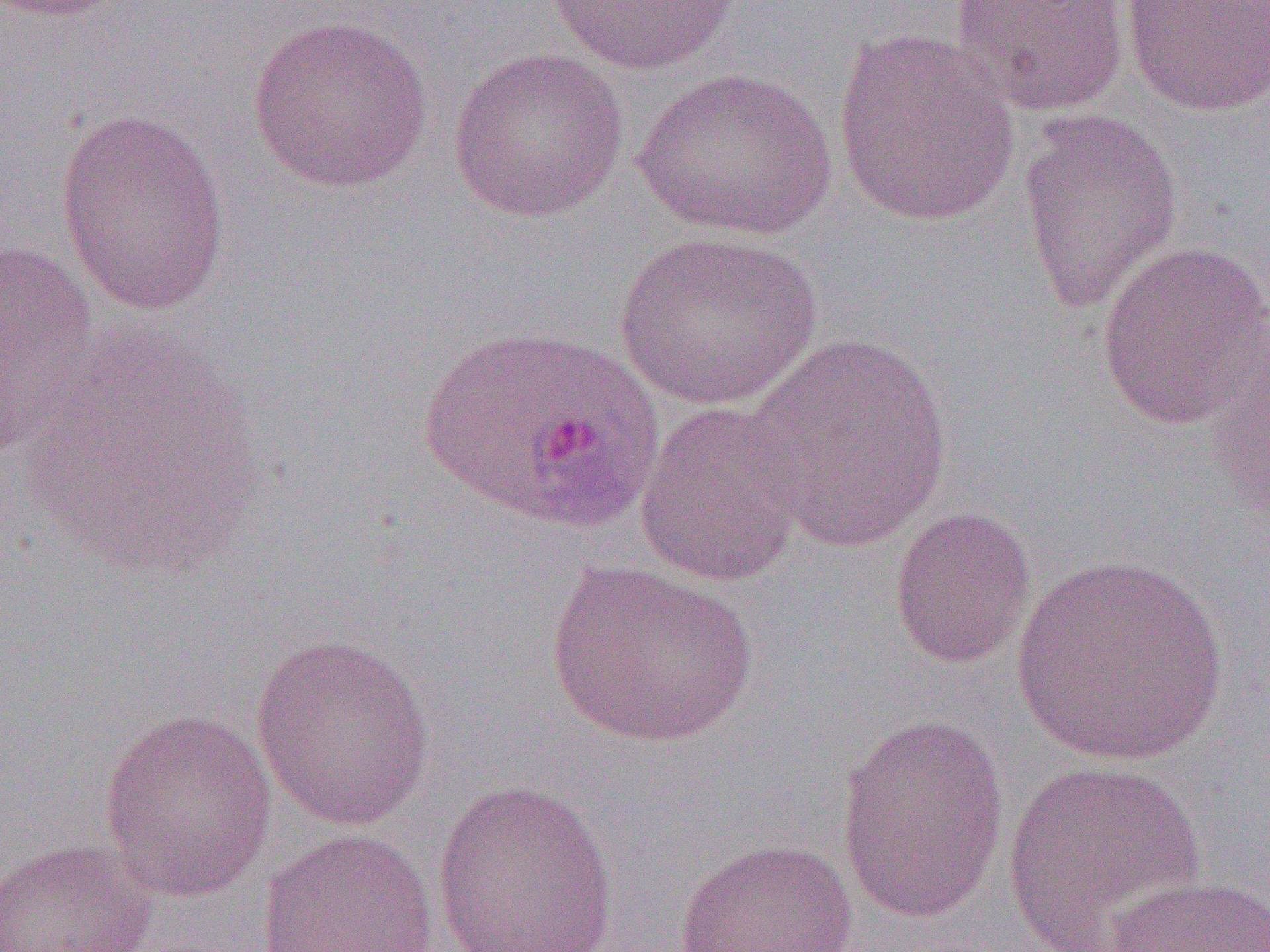

Summary:
  - Coordinate format: approximate bounding boxes as [x1, y1, x2, y2] in pixels
  - Uninfected red blood cell locations: [0, 0, 137, 21], [949, 0, 1130, 118], [1121, 0, 1270, 117], [547, 1, 742, 75], [246, 14, 435, 194], [830, 29, 1022, 229], [447, 46, 630, 223], [632, 66, 839, 242], [1016, 106, 1183, 315], [55, 109, 231, 317], [614, 230, 822, 411], [0, 240, 102, 456], [1096, 240, 1270, 430], [16, 332, 269, 579], [741, 335, 954, 551], [1206, 338, 1270, 525], [634, 400, 811, 590], [888, 505, 1037, 669], [1010, 554, 1230, 766], [541, 559, 761, 749], [249, 633, 436, 832], [100, 706, 278, 902], [835, 712, 1010, 926], [1002, 759, 1207, 950], [431, 778, 620, 952], [257, 826, 439, 952], [0, 837, 158, 952], [674, 838, 860, 952], [1105, 875, 1270, 952]
  - Plasmodium ovale-infected red blood cell locations: [413, 324, 666, 536]
  - Slide-level diagnosis: Plasmodium ovale
  - Preparation: thin blood film
  - Field of view: single
  - Modality: light microscopy
  - Magnification: 1000x
  - Image size: 1270×952 pixels